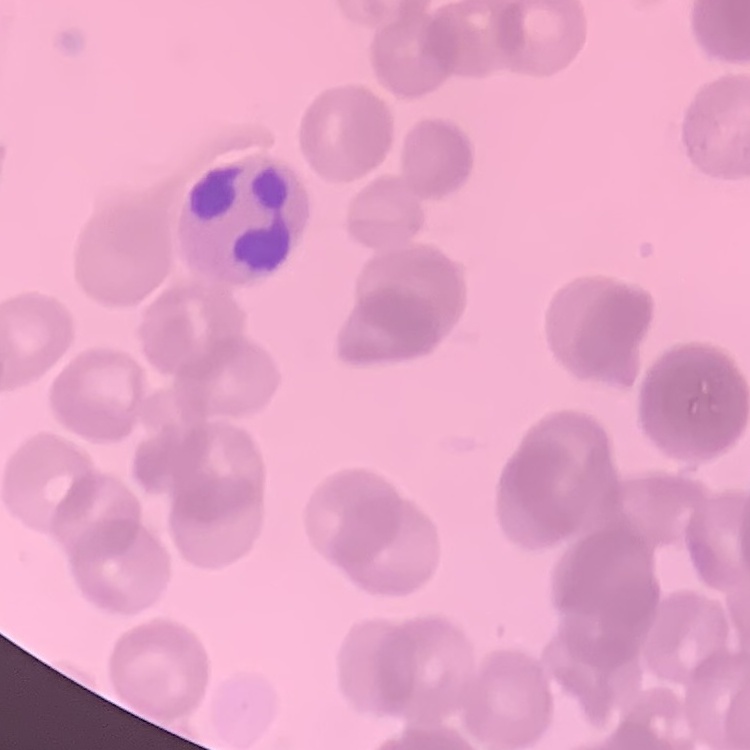

Summary:
  - Erythrocyte morphology: rouleaux formation
  - Image type: square crop of a larger photomicrograph
  - Preparation: thin blood smear
  - Stain: Field's or Giemsa